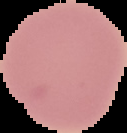
Summary:
  - Image type: segmented cell region with the area outside set to black
  - Image size: 127×133 pixels
  - Preparation: thin blood smear
  - Result: no malaria parasites seen